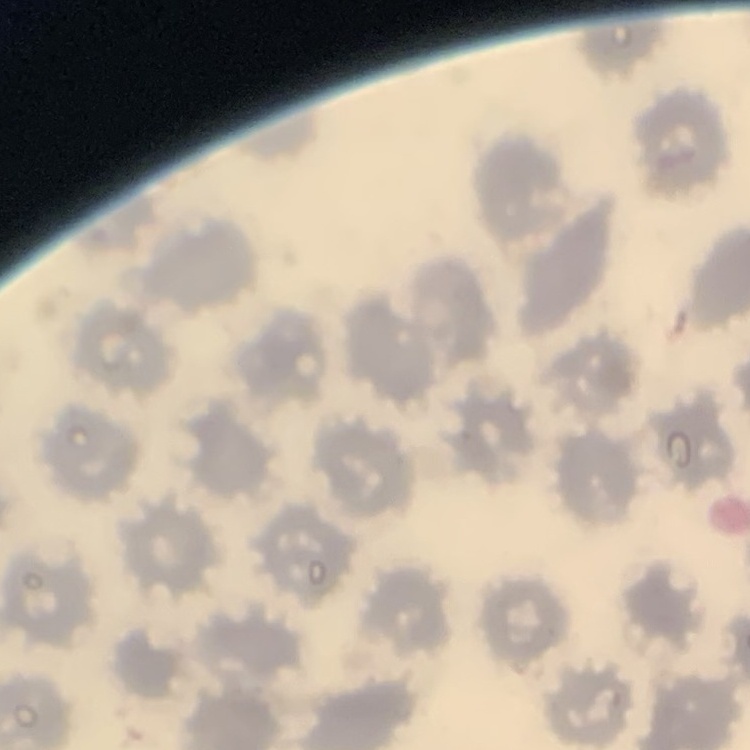

Summary:
  - Red blood cell morphology: no rouleaux formation
  - Stain: Field's or Giemsa
  - Preparation: thin blood smear
  - Image type: one tile cut from a larger photomicrograph